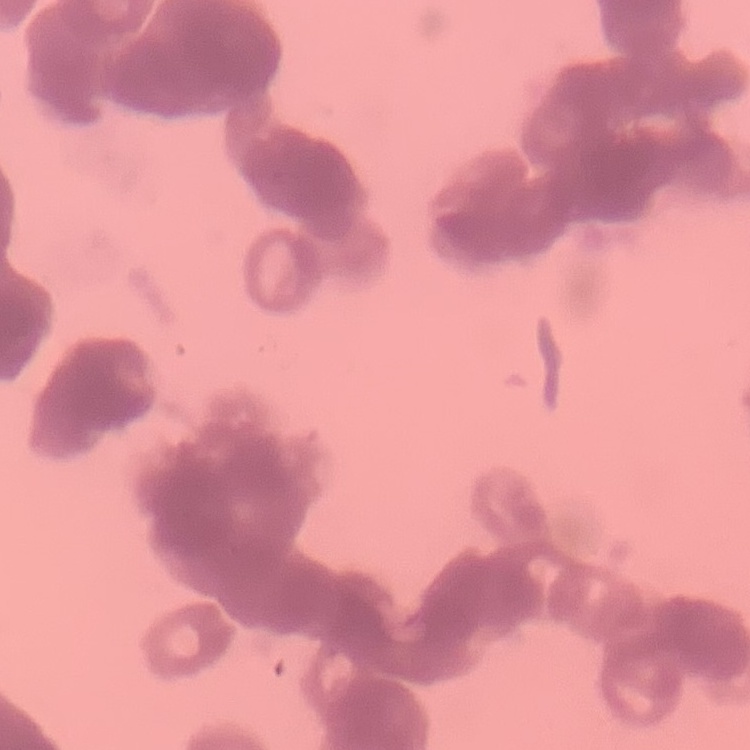

erythrocyte morphology = rouleaux formation
stain = Field's or Giemsa
image type = one tile cut from a larger photomicrograph
preparation = thin blood film